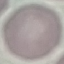

{
  "malaria_status": "uninfected",
  "preparation": "thin blood smear",
  "capture": "smartphone camera at the microscope eyepiece",
  "stain": "Giemsa",
  "image_type": "cell patch, automatically extracted from a larger field of view and resized to 64 × 64 pixels"
}